Outline each blood parasite and name the species.
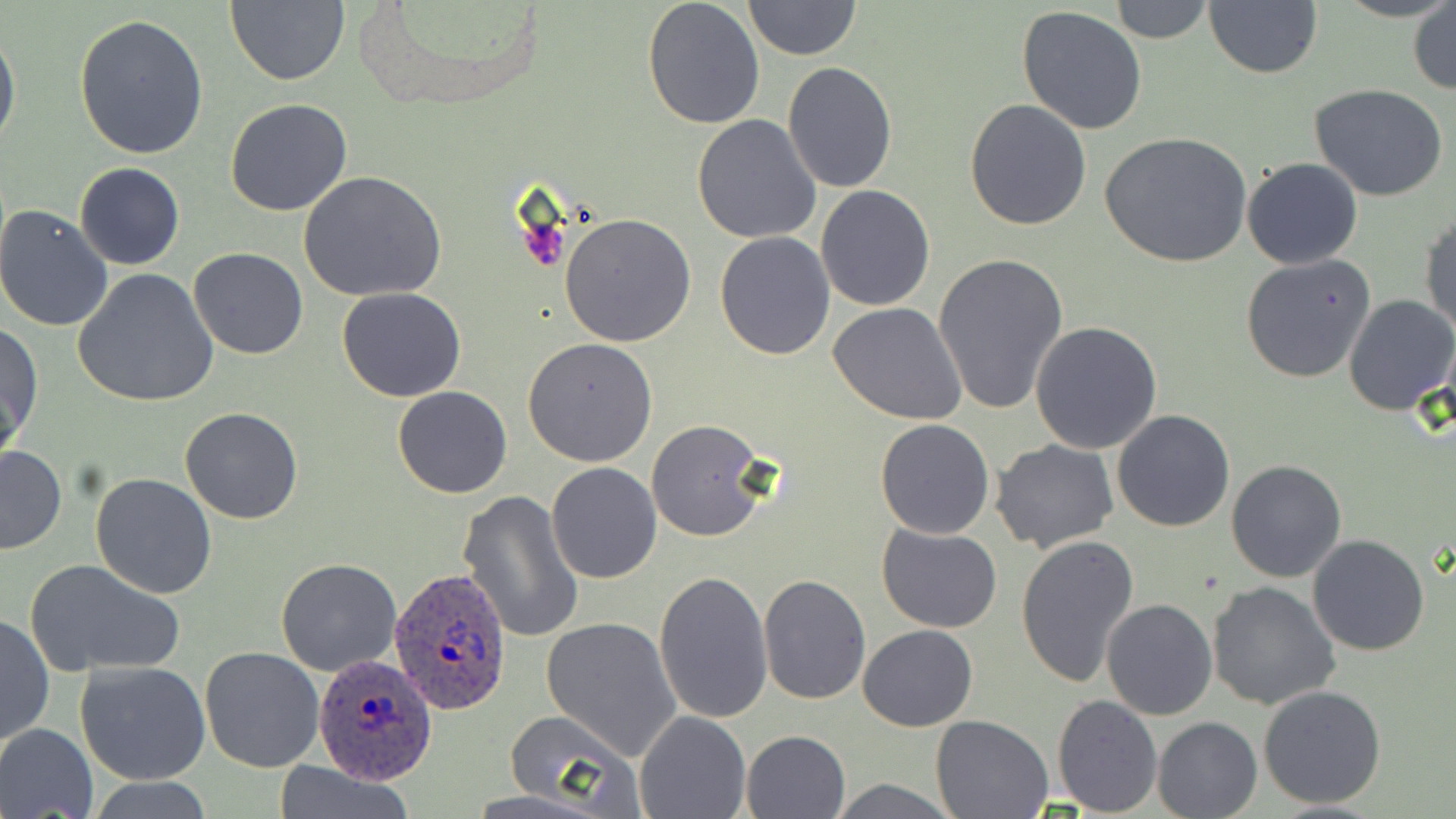
Approximate bounding boxes as [x1, y1, x2, y2] in pixels.
Plasmodium ovale-infected red blood cells: [389, 568, 513, 716], [313, 655, 436, 785].
No Plasmodium falciparum, Plasmodium malariae, Plasmodium vivax, Babesia divergens, or Trypanosoma brucei observed.

slide-level diagnosis = Plasmodium ovale
uninfected red blood cell locations = approximate bounding boxes as [x1, y1, x2, y2] in pixels: [224, 0, 348, 85], [1110, 0, 1213, 43], [641, 1, 766, 132], [743, 1, 861, 59], [1203, 2, 1323, 79], [1408, 3, 1455, 94], [1016, 6, 1149, 135], [73, 14, 208, 160], [0, 25, 20, 154], [784, 61, 897, 194], [1310, 85, 1449, 202], [225, 98, 353, 217], [964, 98, 1092, 230], [692, 115, 821, 243], [1100, 131, 1252, 267], [1242, 158, 1363, 270], [74, 163, 185, 270], [299, 171, 447, 302], [815, 184, 935, 311], [0, 203, 116, 331], [1420, 211, 1455, 337], [560, 212, 696, 346], [714, 231, 836, 359], [189, 248, 308, 361], [932, 252, 1070, 416], [1240, 255, 1376, 383], [72, 270, 219, 407], [337, 287, 467, 402], [1344, 294, 1456, 415], [828, 303, 969, 424], [1030, 321, 1164, 454], [1, 322, 41, 453], [522, 337, 658, 465], [392, 385, 512, 498], [180, 407, 304, 525], [1111, 410, 1235, 532], [874, 418, 995, 539], [646, 420, 769, 541], [990, 439, 1119, 554], [0, 446, 67, 555], [1225, 460, 1347, 583], [547, 462, 661, 584], [91, 472, 217, 598], [458, 490, 584, 642], [877, 525, 1003, 634], [1307, 534, 1429, 657], [1015, 535, 1140, 687], [24, 558, 185, 678], [276, 559, 401, 676], [654, 570, 774, 724], [758, 573, 871, 705], [1207, 581, 1340, 711], [1101, 597, 1217, 720], [0, 613, 54, 750], [542, 616, 682, 760], [857, 624, 979, 731], [199, 646, 325, 773], [76, 660, 211, 785], [1258, 685, 1387, 809], [1051, 694, 1163, 817], [503, 710, 643, 815], [635, 711, 750, 819], [931, 713, 1054, 817], [1153, 716, 1263, 818], [0, 723, 98, 818], [741, 731, 850, 818], [273, 760, 415, 819], [825, 777, 962, 817], [92, 778, 213, 818]
field of view = single
stain = May-Grünwald-Giemsa
magnification = 1000x
preparation = thin blood smear
modality = light microscopy
image size = 1456×819 pixels